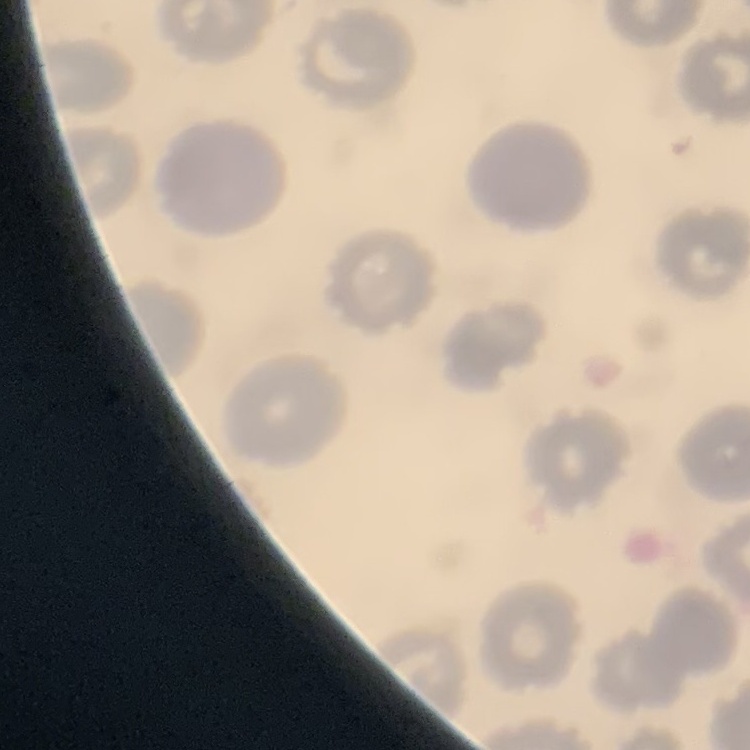
{
  "erythrocyte_morphology": "no rouleaux formation",
  "image_type": "one tile cut from a larger photomicrograph",
  "preparation": "thin blood film",
  "stain": "Field's or Giemsa"
}